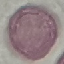
result = negative for malaria parasites
stain = Giemsa
preparation = thin blood smear
capture = smartphone camera at the microscope eyepiece
image type = automatically extracted cell patch, resized to 64 × 64 pixels